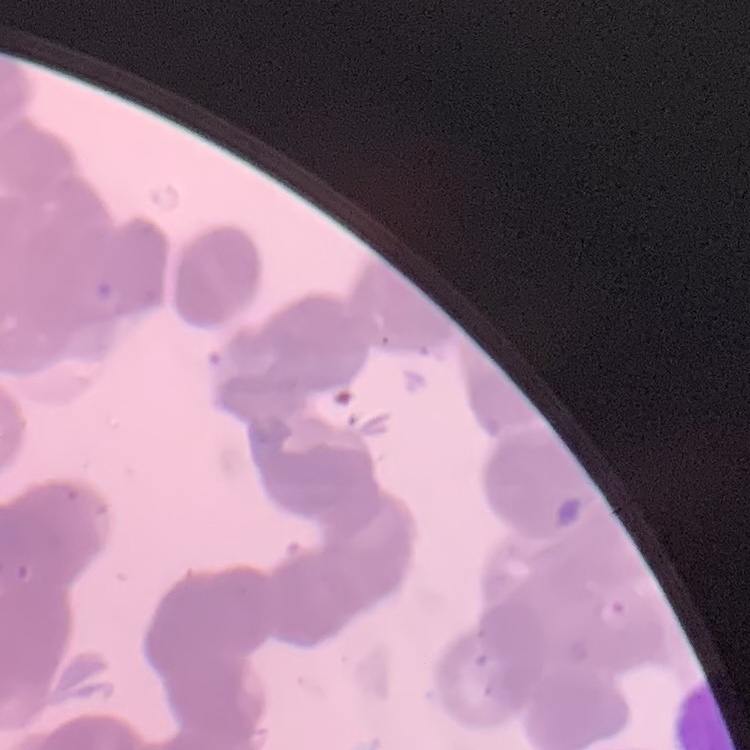 The erythrocytes exhibit rouleaux formation. Thin blood film. Field's or Giemsa stain. One tile cut from a larger photomicrograph.